Assess this cell for malaria.
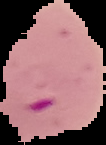

Parasitized.

Summary:
  - Image type: segmented cell region on a black background
  - Preparation: thin blood film
  - Image size: 106×145 pixels